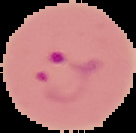
Summary:
  - Image type: cell region segmented out of the field of view; surrounding area masked to black
  - Image size: 136×133 pixels
  - Result: malaria parasites identified
  - Preparation: thin blood film